Give the location of every parasitized red blood cell.
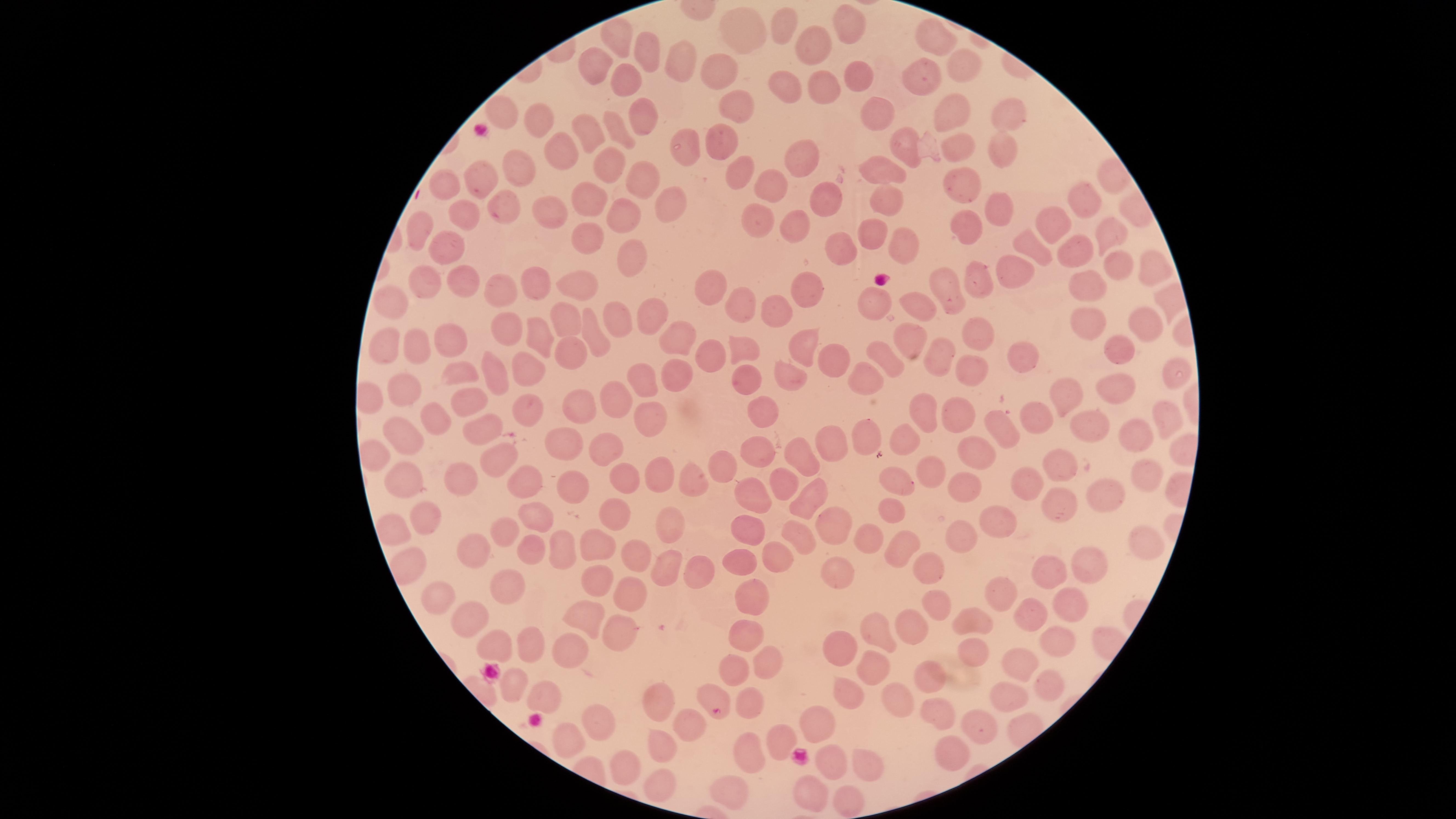

No parasitized red blood cells identified.

Approximate marker points as [x, y] in pixels.
Summary:
  - Uninfected red blood cells: [851, 24], [785, 25], [746, 28], [619, 34], [935, 34], [818, 43], [646, 51], [597, 58], [679, 62], [723, 64], [963, 65], [852, 71], [921, 72], [624, 77], [781, 82], [819, 85], [730, 107], [507, 111], [867, 112], [1011, 112], [640, 114], [547, 116], [947, 116], [619, 129], [723, 129], [593, 132], [681, 140], [900, 146], [958, 148], [1000, 150], [559, 152], [797, 158], [602, 161], [521, 162], [740, 165], [632, 174], [883, 174], [483, 180], [970, 184], [448, 186], [771, 188], [816, 196], [595, 200], [1081, 200], [883, 202], [661, 203], [508, 205], [560, 209], [999, 209], [460, 212], [627, 219], [759, 219], [966, 219], [1059, 220], [798, 222], [420, 231], [873, 231], [1104, 231], [592, 240], [1029, 240], [900, 243], [1071, 246], [841, 247], [451, 251], [626, 256], [1113, 262], [1152, 264], [1014, 270], [583, 278], [975, 279], [464, 280], [427, 281], [538, 282], [807, 284], [1092, 284], [714, 287], [951, 287], [503, 289], [393, 299], [879, 299], [739, 302], [921, 305], [778, 308], [652, 309], [620, 318], [569, 320], [1092, 321], [1144, 321], [592, 329], [972, 330], [509, 333], [534, 333], [675, 334], [453, 336], [908, 338], [381, 346], [1119, 346], [411, 349], [803, 350], [739, 351], [1023, 352], [571, 353], [703, 353], [942, 353], [888, 359], [833, 360], [463, 364], [495, 366], [528, 368], [968, 369], [1169, 369], [795, 372], [678, 373], [648, 376], [747, 376], [870, 378], [1124, 384], [404, 390], [1071, 391], [468, 394], [616, 394], [571, 404], [771, 404], [523, 405], [921, 407], [1027, 410], [435, 411], [959, 417], [652, 418], [1170, 418], [486, 421], [1100, 422], [996, 427], [870, 435], [1141, 435], [402, 440], [904, 441], [560, 442], [832, 442], [601, 444], [979, 449], [756, 453], [496, 455], [803, 457], [1068, 462], [935, 467], [1145, 467], [721, 468], [461, 472], [406, 473], [890, 477], [1027, 477], [524, 478], [662, 480], [778, 480], [623, 481], [696, 482], [564, 483], [962, 483], [751, 494], [805, 494], [1104, 494], [889, 508], [1056, 508], [615, 513], [534, 515], [992, 520], [430, 522], [676, 524], [829, 524], [750, 526], [392, 529], [503, 529], [868, 533], [799, 535], [958, 537], [1145, 539], [595, 541], [561, 542], [897, 545], [478, 548], [532, 550], [630, 555], [741, 556], [772, 557], [409, 562], [662, 564], [1090, 565], [837, 570], [928, 570], [1052, 572], [699, 576], [508, 582], [597, 583], [1003, 588], [628, 590], [749, 593], [441, 594], [936, 601], [1067, 603], [1028, 609], [972, 613], [469, 618], [579, 618], [909, 626], [621, 627], [747, 629], [878, 632], [493, 639], [1051, 643], [526, 645], [843, 648], [972, 649], [565, 654], [1024, 655], [767, 656], [875, 657], [731, 664], [928, 675], [1047, 681], [506, 686], [851, 686], [715, 693], [1013, 693], [543, 694], [752, 697], [895, 699], [657, 703], [935, 711], [812, 718], [592, 719], [686, 721], [974, 722], [663, 737], [777, 738], [564, 740], [743, 751], [952, 751], [869, 761], [629, 764], [826, 766], [657, 779], [727, 786], [807, 789], [843, 798]
  - Image size: 1456×819 pixels
  - Stain: Giemsa
  - Preparation: thin blood film
  - Capture: smartphone photograph through the microscope eyepiece
  - Field of view: single
  - Visible region: circular